Classify this cell by malaria status.
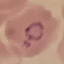
Parasitized.

Acquired by smartphone through the microscope eyepiece. Thin blood film. Cell patch, automatically extracted from a larger field of view and resized to 64 × 64 pixels. Giemsa-stained preparation.